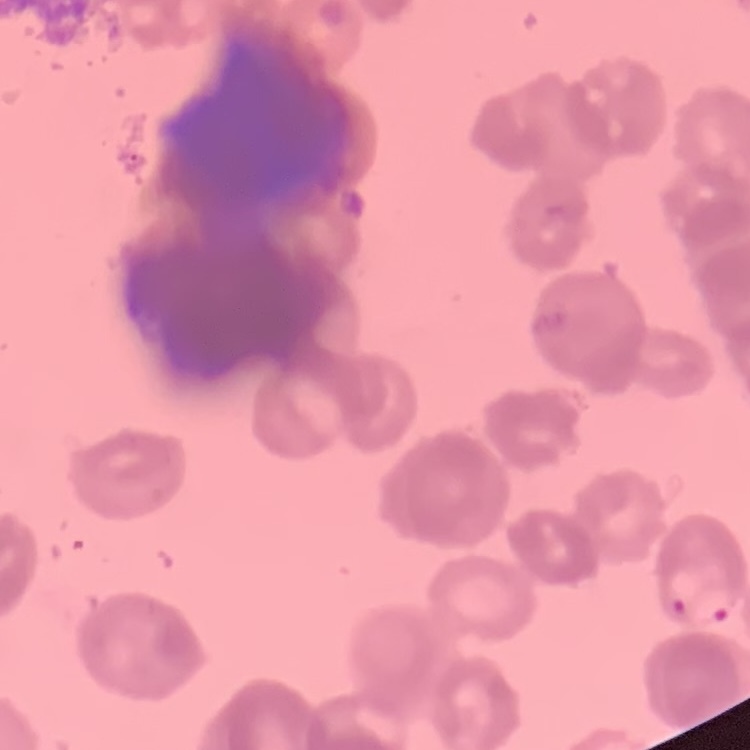

Summary:
  - Red blood cell morphology: rouleaux formation
  - Stain: Field's or Giemsa
  - Image type: square crop of a larger photomicrograph
  - Preparation: thin blood film